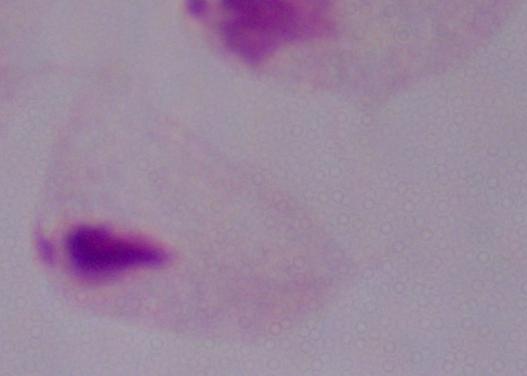
Captured at 1000x magnification. A trichomonad is shown. Micrograph.